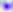

Summary:
  - Modality: micrograph
  - Identification: Toxoplasma gondii
  - Magnification: 400x